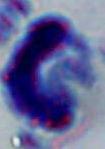

modality = micrograph
magnification = 1000x
identification = leukocyte